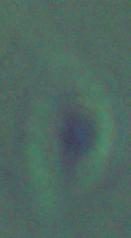
Summary:
  - Modality: photomicrograph
  - Magnification: 1000x
  - Identification: Leishmania